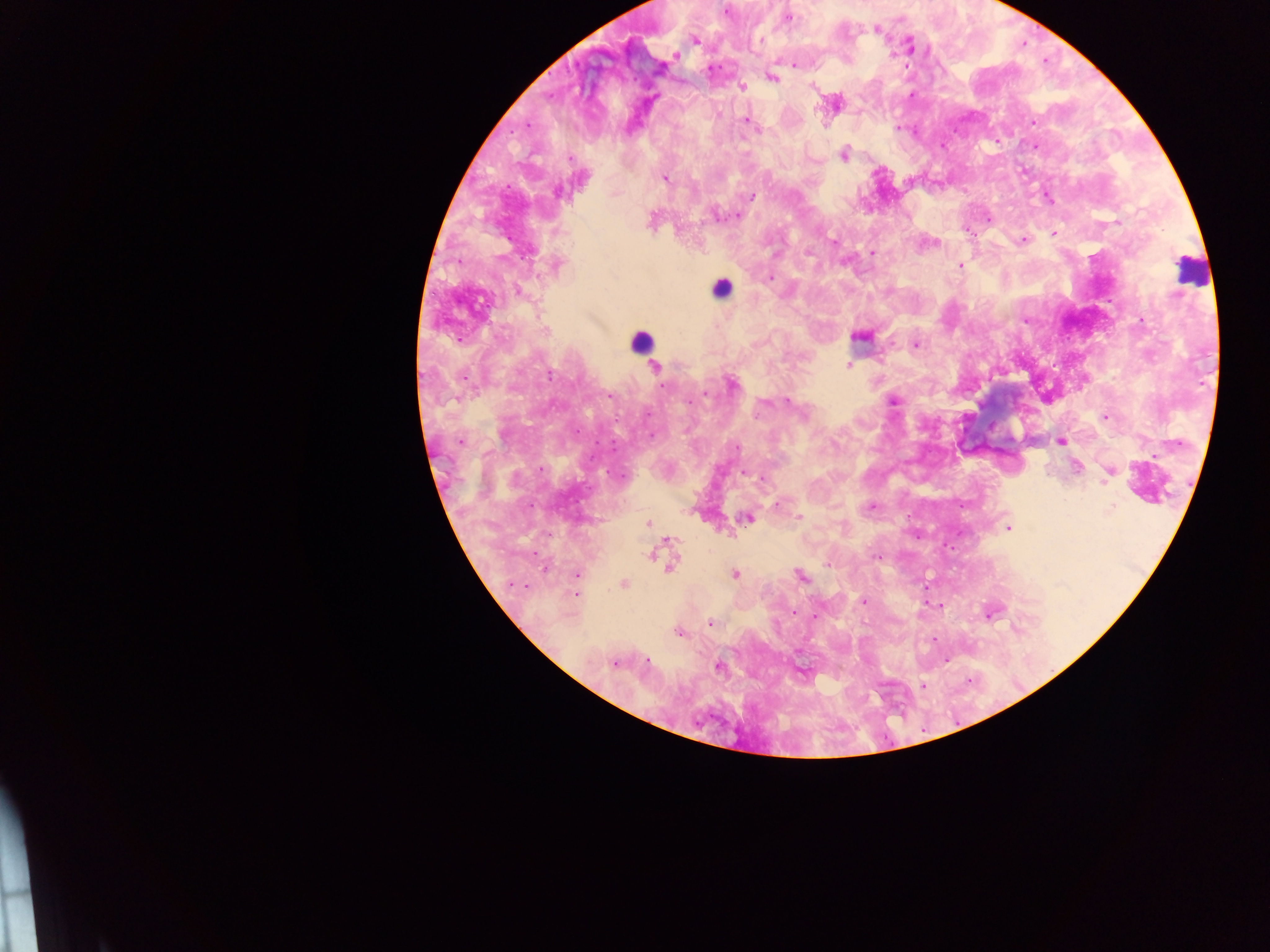
Approximate centers as {x, y} in pixels. Malaria parasite locations: {726, 11}, {789, 18}, {876, 29}, {695, 41}, {760, 41}, {675, 56}, {795, 65}, {780, 73}, {773, 78}, {743, 87}, {813, 88}, {911, 95}, {746, 120}, {1032, 121}, {898, 129}, {845, 153}, {665, 178}, {558, 193}, {751, 196}, {1048, 197}, {737, 216}, {988, 218}, {653, 219}, {1116, 221}, {1054, 234}, {1023, 240}, {834, 241}, {935, 243}, {871, 253}, {557, 264}, {960, 266}, {770, 278}, {518, 292}, {545, 330}, {860, 335}, {917, 344}, {848, 365}, {655, 367}, {550, 375}, {732, 384}, {662, 386}, {706, 393}, {610, 396}, {688, 401}, {894, 401}, {788, 402}, {648, 414}, {802, 414}, {1105, 417}, {459, 442}, {1060, 442}, {737, 447}, {1077, 467}, {540, 469}, {1110, 472}, {746, 473}, {761, 478}, {1106, 478}, {776, 505}, {870, 507}, {1112, 507}, {799, 517}, {747, 518}, {648, 523}, {1009, 528}, {670, 541}, {649, 555}, {877, 557}, {827, 565}, {671, 567}, {544, 569}, {735, 574}, {577, 575}, {800, 577}, {624, 584}, {513, 585}, {576, 594}, {863, 602}, {795, 612}, {991, 613}, {816, 616}, {711, 623}, {1017, 628}, {679, 632}, {933, 640}, {947, 660}, {647, 661}, {614, 664}, {718, 667}, {802, 673}, {922, 687}. Leukocyte locations: {1190, 271}, {721, 289}, {642, 341}. Mobile-phone photograph taken through the microscope. Image is 1270×952 pixels. Single field of view. Collected in Ghana. Thick blood smear.